Give the position of every malaria parasite.
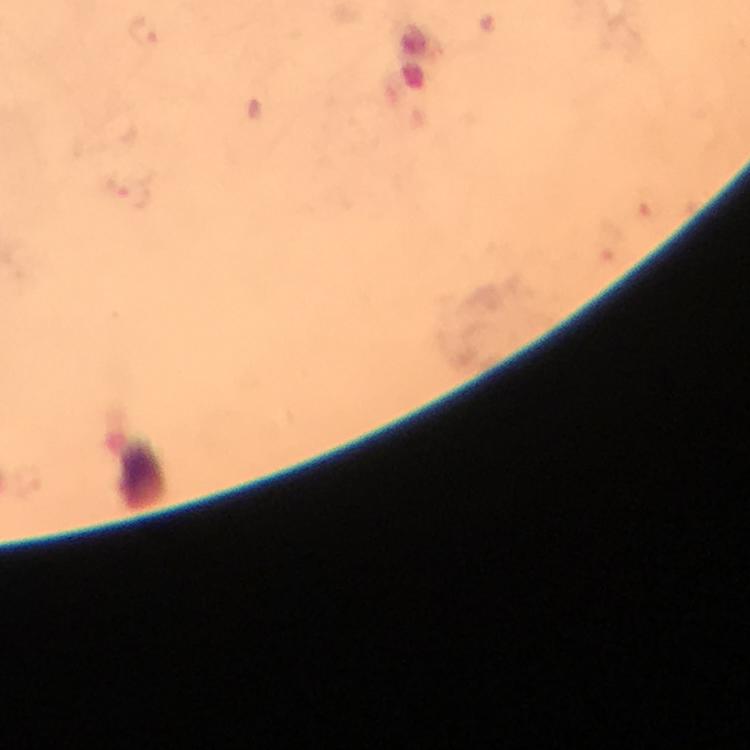

Approximate object centers, in pixels from the top-left corner.
Malaria parasites: (x=146, y=31).

Summary:
  - Context: from a malaria diagnostic workup
  - Immersion oil: used
  - Cropped from: one field of view
  - Stain: Giemsa
  - Magnification: 100x
  - Image size: 750×750 pixels
  - Preparation: thick blood smear
  - Capture: smartphone camera through the microscope